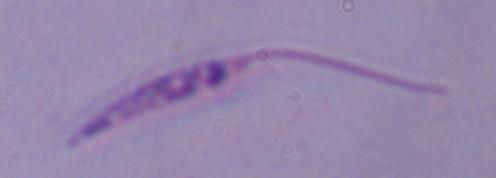
Summary:
  - Modality: micrograph
  - Magnification: 1000x
  - Identification: Leishmania